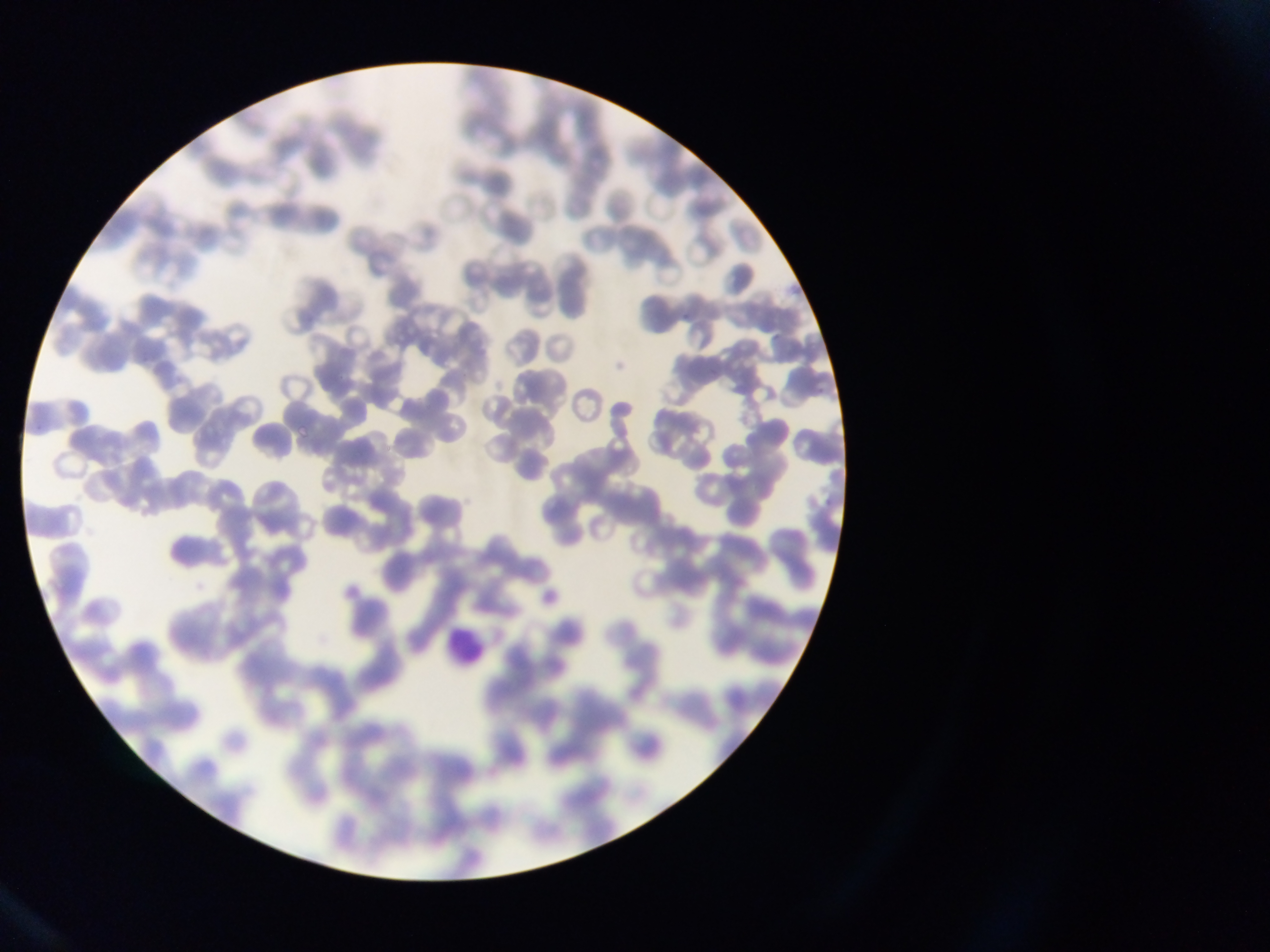

{
  "image_size": "1270×952 pixels",
  "plasmodium_parasite_locations": "approximate bounding boxes as [left, top, right, bottom] in pixels: [34, 421, 46, 432], [297, 424, 311, 439]",
  "country": "Ghana",
  "field_of_view": "single",
  "capture": "mobile-phone photograph through a microscope",
  "leukocyte_locations": "approximate bounding boxes as [left, top, right, bottom] in pixels: [447, 630, 485, 660]",
  "preparation": "thin blood smear"
}